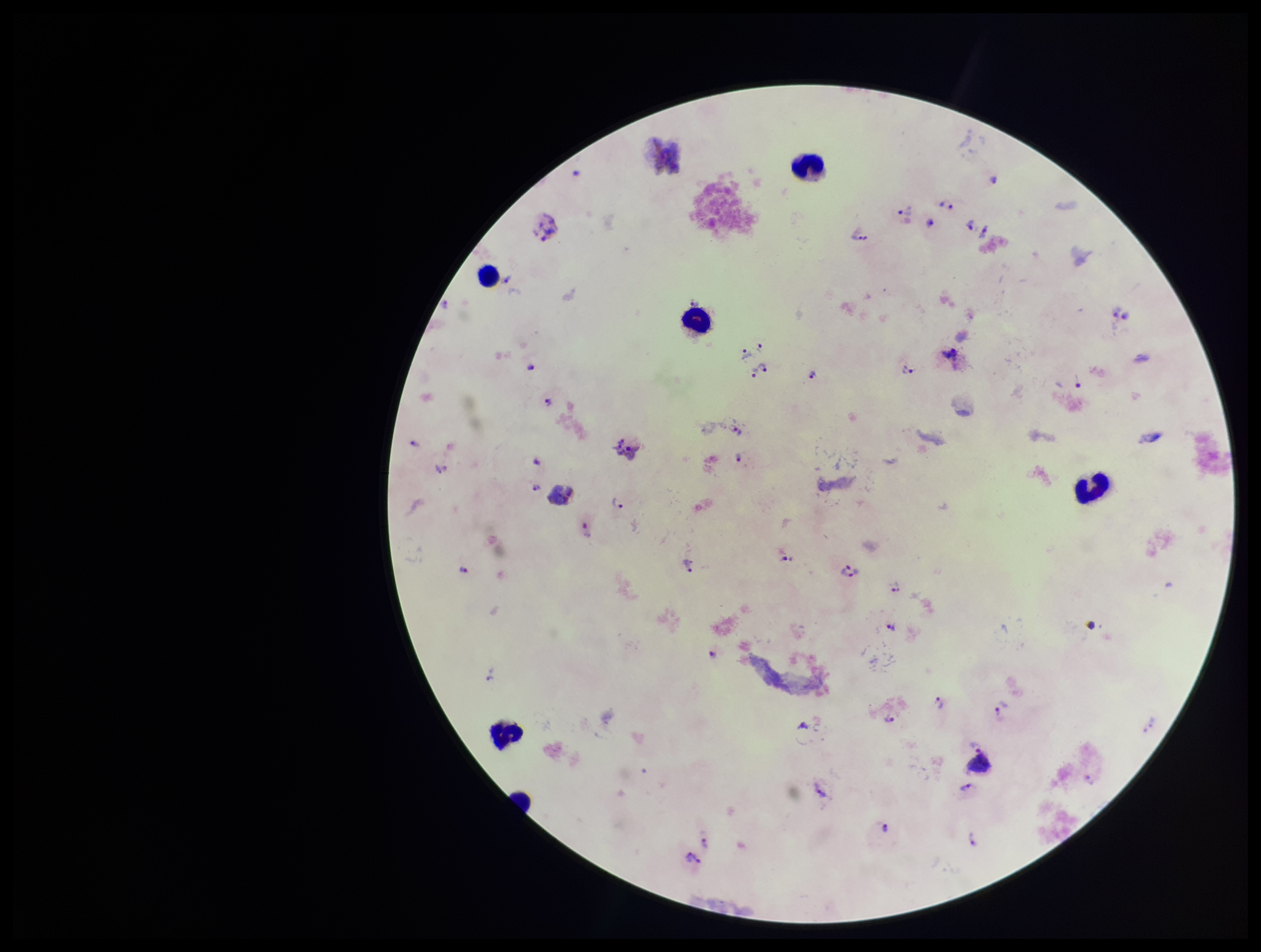
Species reported for this patient: Plasmodium vivax. Patient malaria status: positive. Preparation: thick. Stained with Giemsa. Plasmodium parasites: seen. Image is 1261×952 pixels. One field from this slide. Leukocyte count: 5. Photographed through the microscope eyepiece with a smartphone camera. Parasite count: 36.